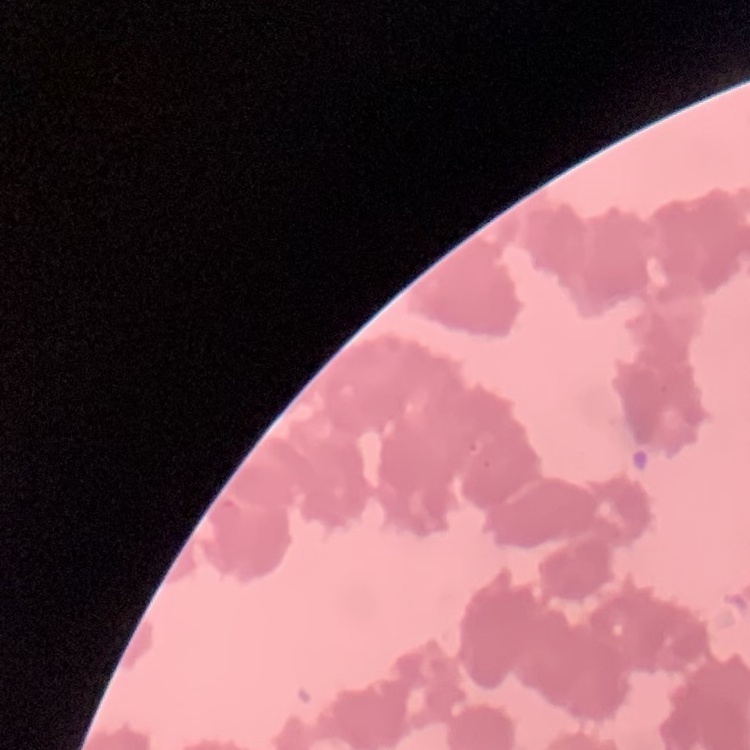
{
  "red_blood_cell_morphology": "rouleaux formation",
  "image_type": "square crop of a larger photomicrograph",
  "stain": "Field's or Giemsa",
  "preparation": "thin blood film"
}